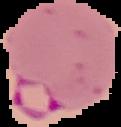

malaria_status: parasitized
preparation: thin blood film
image_type: cell region segmented out of the field of view; surrounding area masked to black
image_size: 121×127 pixels